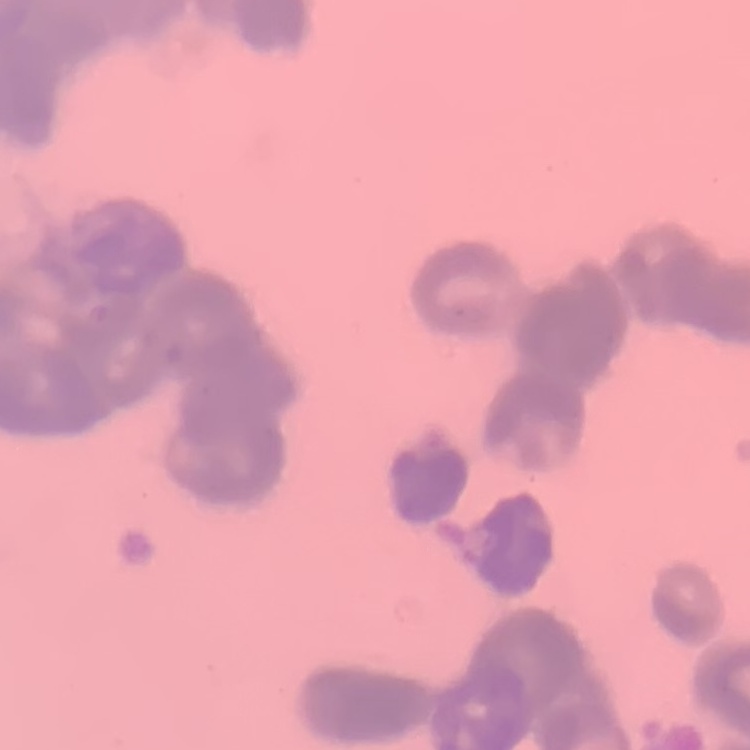

Summary:
  - Erythrocyte morphology: rouleaux formation
  - Preparation: thin blood smear
  - Image type: one tile cut from a larger photomicrograph
  - Stain: Field's or Giemsa